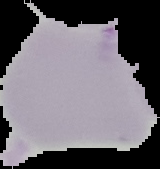
From a thin blood smear. Image is 160×169 pixels. Segmented cell region on a black background. Result: no malaria parasites detected.